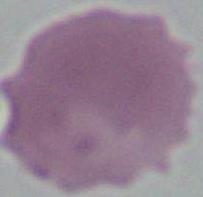
Summary:
  - Magnification: 1000x
  - Modality: micrograph
  - Identification: erythrocyte